Identify the parasite.
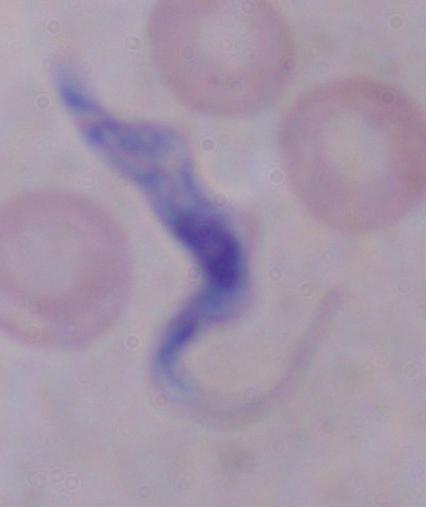

This is a trypanosome.

Photomicrograph. Captured at 1000x magnification.